State which parasite is depicted.
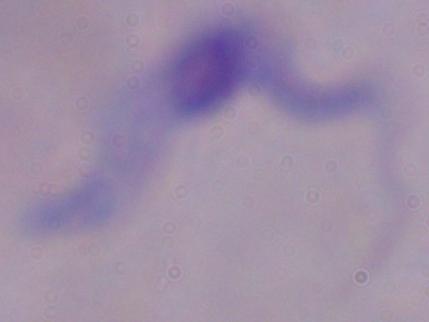

This is a trypanosome.

Summary:
  - Magnification: 1000x
  - Modality: photomicrograph